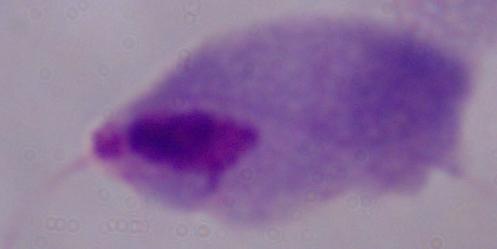
A trichomonad is shown. Captured at 1000x magnification. Micrograph.